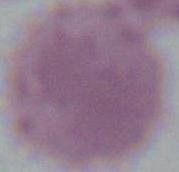
A red blood cell is seen. Micrograph. 1000x magnification.